Outline each blood parasite and name the species.
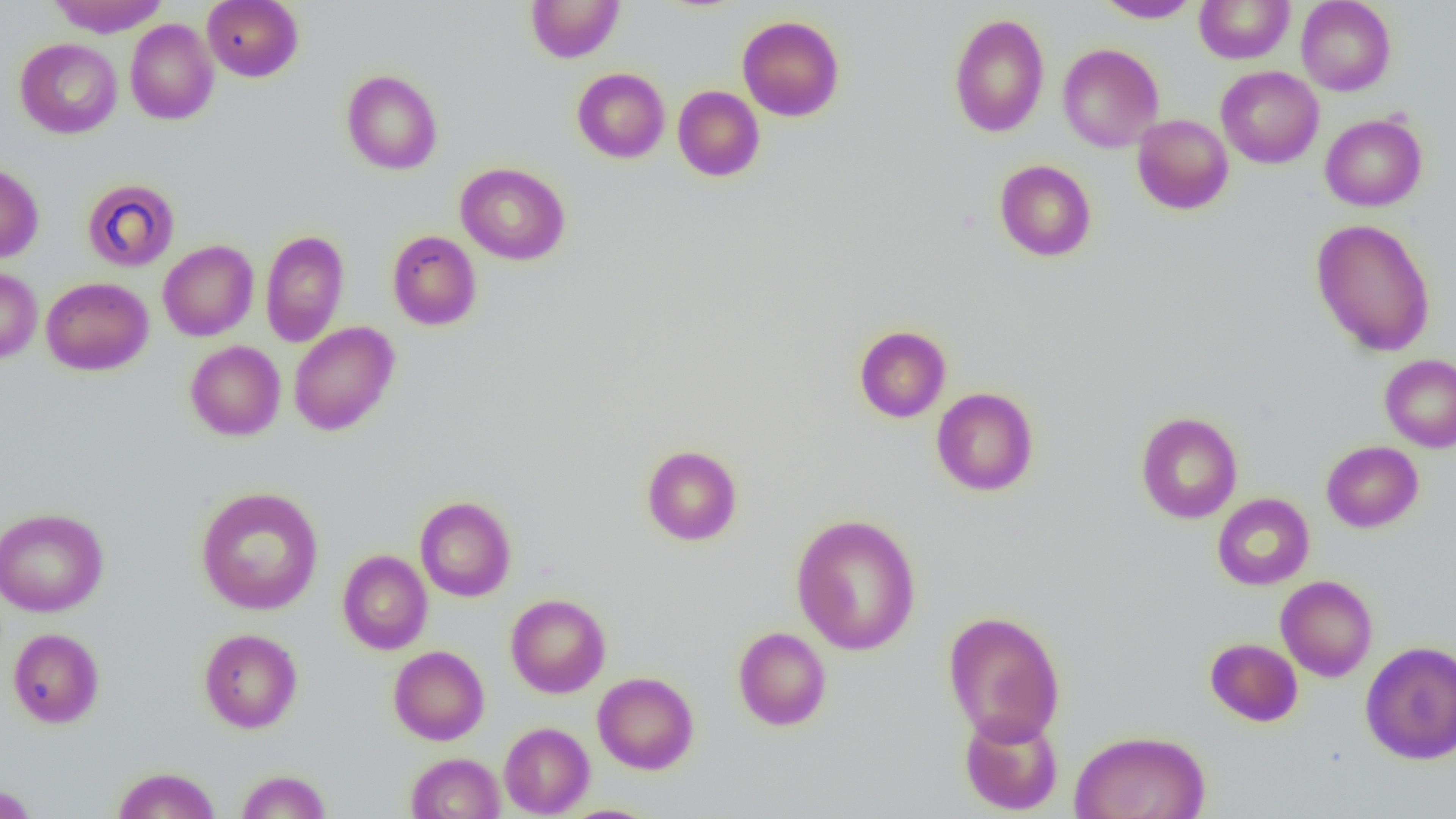
No blood parasites observed.

Summary:
  - Coordinate format: approximate bounding boxes as named x1/y1/x2/y2 corners in pixels
  - Uninfected red blood cell locations: (x1=47, y1=0, x2=170, y2=37), (x1=202, y1=0, x2=303, y2=82), (x1=526, y1=0, x2=624, y2=63), (x1=1095, y1=0, x2=1200, y2=22), (x1=1296, y1=0, x2=1396, y2=95), (x1=1194, y1=1, x2=1295, y2=64), (x1=949, y1=13, x2=1049, y2=137), (x1=737, y1=16, x2=845, y2=121), (x1=125, y1=19, x2=219, y2=125), (x1=15, y1=38, x2=122, y2=139), (x1=1057, y1=43, x2=1164, y2=152), (x1=1216, y1=66, x2=1324, y2=169), (x1=572, y1=68, x2=670, y2=163), (x1=341, y1=70, x2=443, y2=174), (x1=672, y1=86, x2=765, y2=181), (x1=1320, y1=113, x2=1427, y2=211), (x1=1132, y1=114, x2=1234, y2=215), (x1=995, y1=159, x2=1096, y2=262), (x1=0, y1=162, x2=43, y2=263), (x1=455, y1=162, x2=571, y2=265), (x1=82, y1=178, x2=180, y2=271), (x1=1311, y1=218, x2=1435, y2=356), (x1=260, y1=229, x2=349, y2=347), (x1=387, y1=230, x2=481, y2=330), (x1=158, y1=239, x2=259, y2=341), (x1=0, y1=267, x2=42, y2=364), (x1=41, y1=277, x2=154, y2=375), (x1=288, y1=321, x2=399, y2=435), (x1=854, y1=325, x2=951, y2=423), (x1=185, y1=341, x2=286, y2=440), (x1=1380, y1=353, x2=1456, y2=453), (x1=931, y1=387, x2=1039, y2=497), (x1=1135, y1=411, x2=1243, y2=523), (x1=1321, y1=440, x2=1423, y2=532), (x1=642, y1=444, x2=742, y2=545), (x1=195, y1=486, x2=324, y2=615), (x1=1213, y1=493, x2=1314, y2=590), (x1=415, y1=496, x2=516, y2=601), (x1=0, y1=507, x2=109, y2=617), (x1=790, y1=513, x2=922, y2=656), (x1=337, y1=549, x2=432, y2=655), (x1=1276, y1=576, x2=1377, y2=682), (x1=506, y1=594, x2=611, y2=698), (x1=942, y1=610, x2=1065, y2=746), (x1=733, y1=626, x2=832, y2=731), (x1=7, y1=628, x2=104, y2=728), (x1=199, y1=628, x2=302, y2=733), (x1=1205, y1=638, x2=1303, y2=726), (x1=1360, y1=640, x2=1456, y2=764), (x1=389, y1=645, x2=489, y2=745), (x1=592, y1=672, x2=699, y2=774), (x1=959, y1=710, x2=1063, y2=816), (x1=499, y1=722, x2=594, y2=817), (x1=1070, y1=729, x2=1211, y2=819), (x1=406, y1=752, x2=505, y2=818), (x1=112, y1=766, x2=220, y2=819), (x1=236, y1=769, x2=331, y2=818), (x1=0, y1=783, x2=39, y2=819)
  - Slide-level diagnosis: no evidence of blood parasites
  - Magnification: 1000x
  - Field of view: single
  - Preparation: thin blood film
  - Modality: optical microscopy
  - Image size: 1456×819 pixels